Comment on the morphology of the erythrocytes.
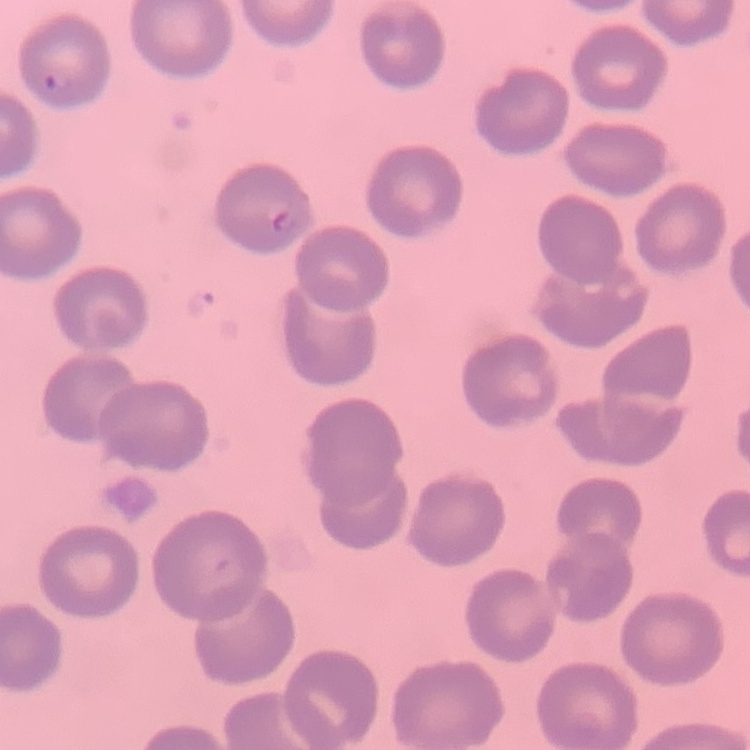

No rouleaux formation.

Thin peripheral smear. Square crop of a larger photomicrograph. Field's or Giemsa stain.